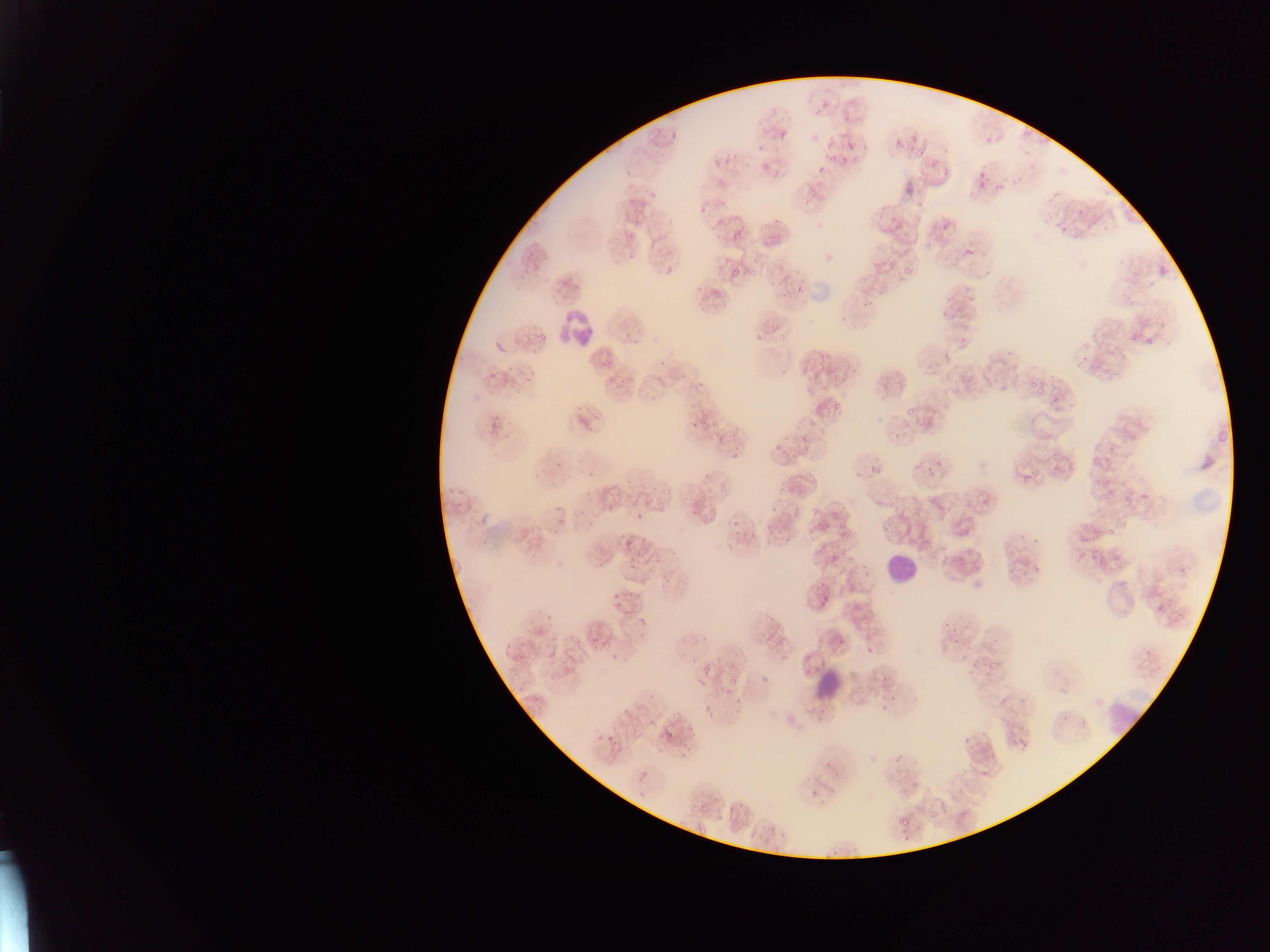 Approximate bounding boxes as left top right bottom in pixels. Leukocyte locations: 553 303 594 350; 886 550 921 588; 1106 697 1141 738. Malaria parasite locations: 812 103 826 117; 776 130 788 140; 669 133 677 139; 909 134 919 142; 824 141 831 150; 893 141 904 151; 843 142 854 152; 756 143 764 152; 713 158 722 167; 761 163 769 171; 817 166 825 173; 966 248 975 256; 729 270 739 280; 790 282 804 296; 657 357 668 367; 695 384 705 393; 832 396 843 413; 578 416 589 426; 690 421 697 431; 771 435 782 449; 727 445 743 459; 925 452 943 479; 866 461 886 475; 584 471 597 483; 634 511 645 521; 730 517 741 527; 823 523 831 531; 1106 528 1113 536; 840 530 848 539; 622 539 632 549; 829 554 838 563; 611 592 621 602; 758 673 772 681; 694 678 706 684; 728 679 740 688; 885 686 895 708; 663 730 672 740; 606 736 616 742 | approximate x y pixel centers of objects too small to bound: 1018 180; 868 650. Single field of view. Image is 1270×952 pixels. Mobile-phone photograph taken through the microscope. Collected in Ghana. Thin blood smear.